Give the extent of all Plasmodium falciparum-infected red blood cells.
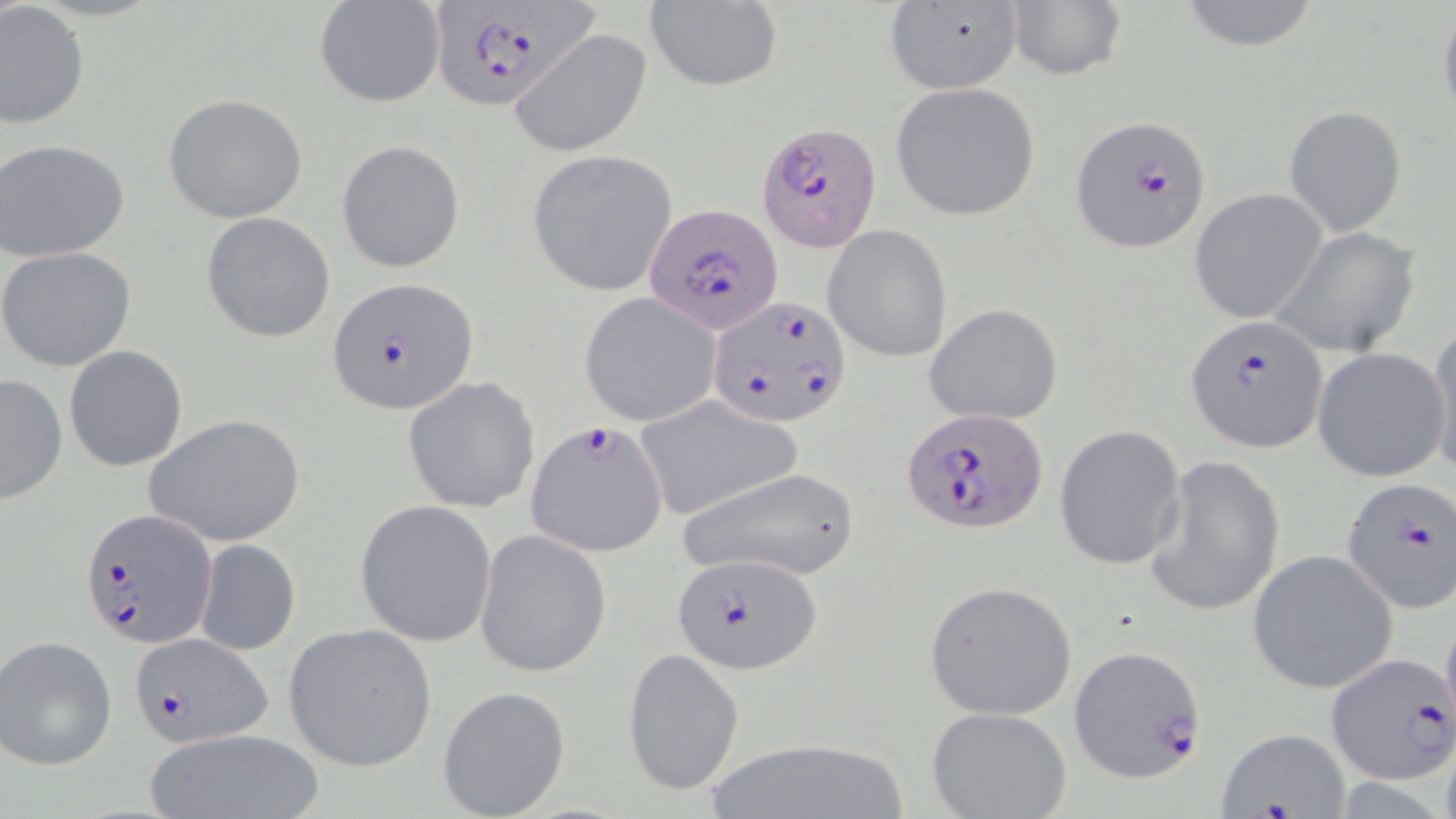

Approximate bounding boxes as named x1/y1/x2/y2 corners in pixels.
Plasmodium falciparum-infected red blood cells: (x1=431, y1=1, x2=591, y2=109), (x1=1068, y1=114, x2=1213, y2=253), (x1=757, y1=121, x2=885, y2=253), (x1=646, y1=203, x2=785, y2=336), (x1=329, y1=276, x2=478, y2=415), (x1=710, y1=295, x2=851, y2=427), (x1=1186, y1=315, x2=1326, y2=452), (x1=901, y1=408, x2=1046, y2=534), (x1=525, y1=421, x2=669, y2=558), (x1=1340, y1=477, x2=1456, y2=614), (x1=81, y1=506, x2=217, y2=650), (x1=672, y1=552, x2=821, y2=676), (x1=130, y1=633, x2=273, y2=747), (x1=1069, y1=645, x2=1205, y2=783), (x1=1325, y1=653, x2=1455, y2=784).

slide-level diagnosis = Plasmodium falciparum
uninfected red blood cell locations = approximate bounding boxes as named x1/y1/x2/y2 corners in pixels: (x1=1174, y1=0, x2=1325, y2=52), (x1=644, y1=1, x2=781, y2=92), (x1=882, y1=2, x2=1024, y2=95), (x1=1004, y1=2, x2=1127, y2=84), (x1=0, y1=3, x2=89, y2=133), (x1=313, y1=3, x2=446, y2=110), (x1=1438, y1=3, x2=1456, y2=127), (x1=509, y1=28, x2=653, y2=159), (x1=888, y1=81, x2=1043, y2=222), (x1=164, y1=93, x2=307, y2=223), (x1=1284, y1=105, x2=1406, y2=236), (x1=1, y1=138, x2=131, y2=261), (x1=336, y1=140, x2=465, y2=273), (x1=527, y1=150, x2=679, y2=297), (x1=1190, y1=188, x2=1328, y2=325), (x1=201, y1=212, x2=334, y2=343), (x1=823, y1=225, x2=953, y2=363), (x1=1271, y1=227, x2=1423, y2=357), (x1=1, y1=247, x2=136, y2=372), (x1=578, y1=294, x2=718, y2=426), (x1=923, y1=303, x2=1063, y2=427), (x1=1426, y1=328, x2=1456, y2=476), (x1=64, y1=346, x2=188, y2=472), (x1=1313, y1=347, x2=1451, y2=483), (x1=0, y1=374, x2=67, y2=503), (x1=402, y1=375, x2=540, y2=513), (x1=634, y1=398, x2=799, y2=522), (x1=143, y1=413, x2=306, y2=547), (x1=1053, y1=425, x2=1186, y2=571), (x1=1144, y1=455, x2=1286, y2=617), (x1=675, y1=465, x2=862, y2=583), (x1=355, y1=500, x2=497, y2=647), (x1=474, y1=530, x2=613, y2=678), (x1=194, y1=538, x2=301, y2=655), (x1=1246, y1=549, x2=1399, y2=695), (x1=923, y1=580, x2=1077, y2=719), (x1=1440, y1=607, x2=1456, y2=734), (x1=282, y1=622, x2=438, y2=772), (x1=1, y1=635, x2=118, y2=769), (x1=623, y1=648, x2=744, y2=798), (x1=437, y1=685, x2=571, y2=818), (x1=926, y1=707, x2=1073, y2=819), (x1=142, y1=728, x2=325, y2=819), (x1=1212, y1=728, x2=1354, y2=818), (x1=695, y1=737, x2=914, y2=819)
stain = May-Grünwald-Giemsa
magnification = 1000x
field of view = one of a larger specimen
modality = light microscopy
preparation = thin blood film
image size = 1456×819 pixels